Give the position of every Plasmodium parasite visible.
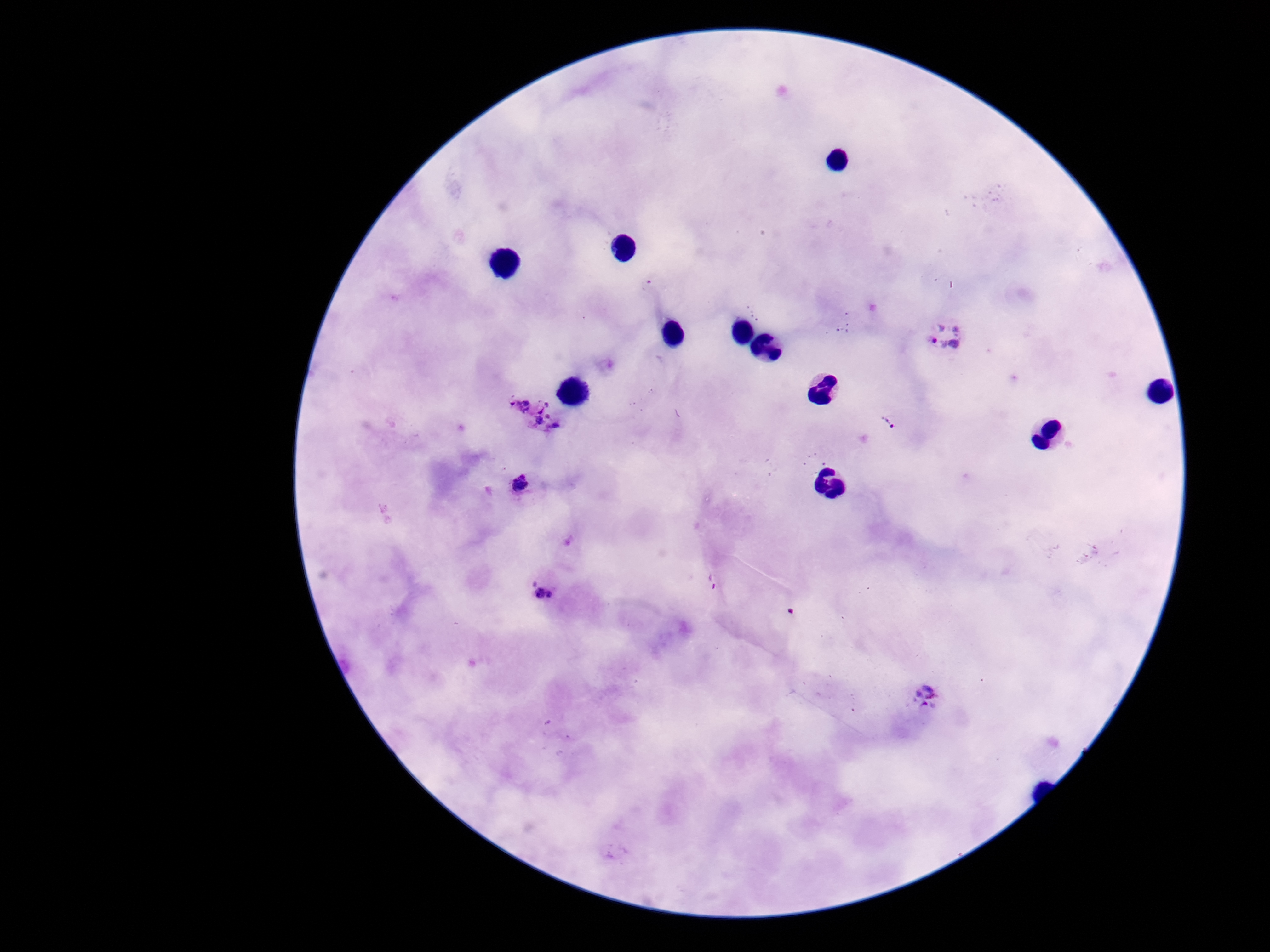
Approximate centers as {x, y} in pixels.
Plasmodium parasites: {945, 335}, {532, 412}, {892, 425}, {521, 485}, {714, 581}, {544, 584}, {926, 700}.

field of view = one from this slide
patient malaria status = infected
image size = 1270×952 pixels
magnification = 100x
capture = smartphone camera through the microscope eyepiece
preparation = thick blood film
stain = Giemsa